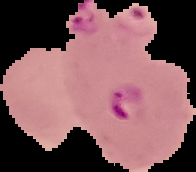
Image is 196×172 pixels. From a thin blood film. Malaria status: parasitized. Segmented cell region on a black background.